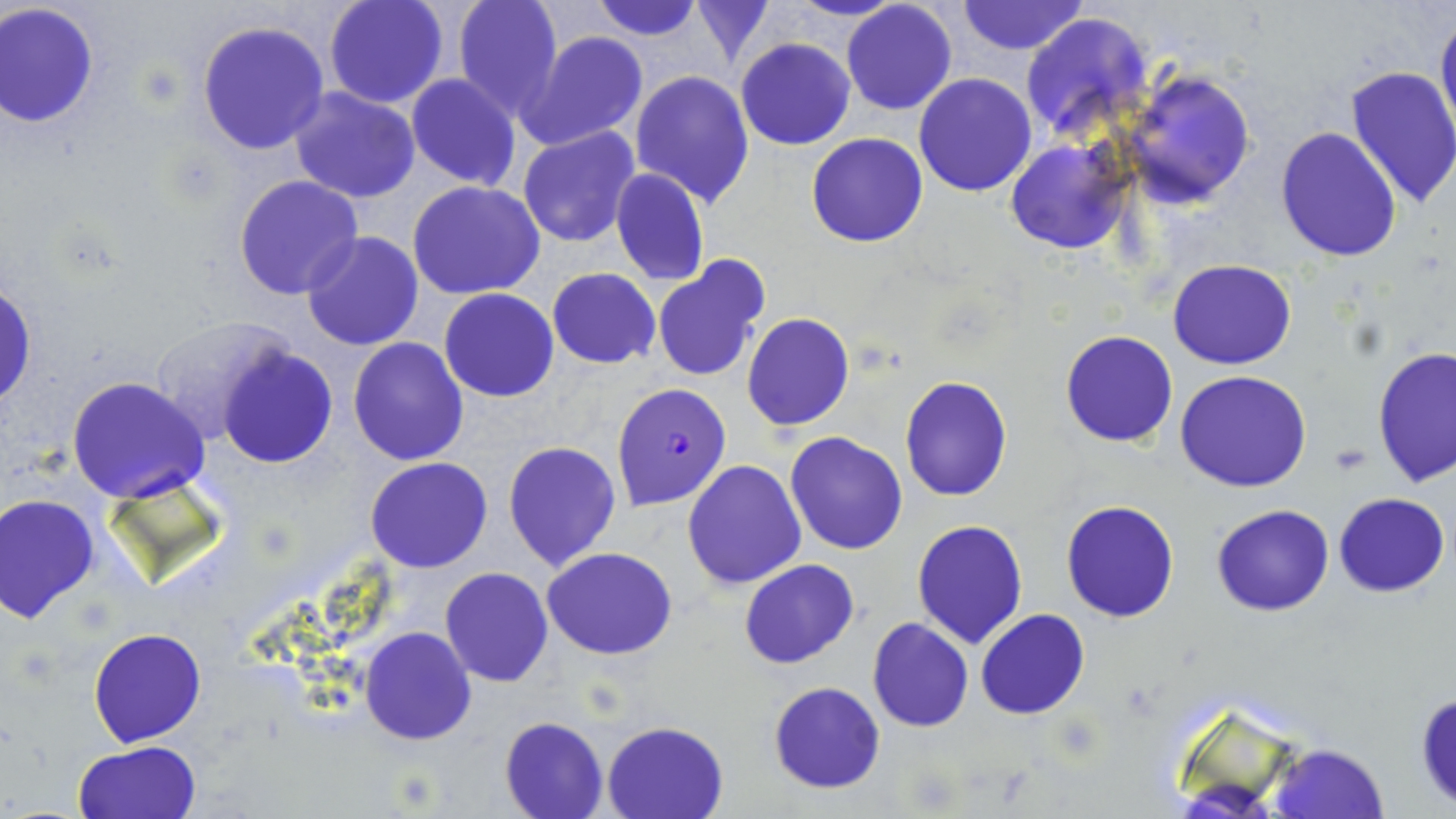

{
  "slide_level_diagnosis": "Plasmodium falciparum",
  "modality": "light microscopy",
  "stain": "May-Grünwald-Giemsa",
  "image_size": "1456×819 pixels",
  "plasmodium_falciparum_infected_red_blood_cell_locations": "approximate bounding boxes as [x1, y1, x2, y2] in pixels: [612, 382, 731, 509]",
  "field_of_view": "one of a larger specimen",
  "preparation": "thin blood film",
  "magnification": "1000x",
  "uninfected_red_blood_cell_locations": "approximate bounding boxes as [x1, y1, x2, y2] in pixels: [324, 0, 449, 108], [453, 0, 564, 119], [588, 0, 707, 42], [689, 0, 777, 68], [788, 0, 907, 22], [841, 1, 957, 116], [957, 1, 1088, 55], [0, 2, 101, 129], [1435, 7, 1456, 143], [1021, 11, 1156, 143], [196, 19, 330, 156], [518, 31, 650, 151], [736, 38, 855, 151], [1345, 66, 1456, 210], [630, 69, 755, 209], [1120, 70, 1256, 208], [915, 73, 1037, 194], [406, 74, 521, 190], [289, 86, 420, 204], [516, 126, 639, 248], [1275, 127, 1402, 264], [807, 133, 928, 247], [1006, 138, 1134, 255], [610, 168, 709, 287], [233, 175, 363, 300], [409, 182, 547, 299], [301, 231, 423, 351], [652, 257, 769, 382], [1169, 260, 1297, 369], [547, 267, 660, 370], [1, 280, 37, 410], [440, 288, 559, 402], [741, 313, 854, 432], [148, 316, 298, 443], [1060, 330, 1179, 448], [348, 337, 469, 466], [218, 344, 339, 469], [1372, 347, 1454, 489], [1174, 371, 1313, 494], [66, 376, 210, 504], [900, 376, 1012, 502], [784, 430, 909, 557], [502, 441, 622, 574], [366, 456, 492, 572], [682, 459, 807, 589], [1334, 492, 1451, 597], [0, 494, 99, 622], [1060, 499, 1180, 622], [1211, 504, 1335, 616], [912, 519, 1029, 649], [542, 547, 677, 659], [739, 558, 859, 669], [440, 567, 553, 687], [974, 609, 1089, 720], [867, 617, 973, 732], [359, 627, 477, 745], [88, 628, 206, 747], [768, 681, 886, 794], [1414, 689, 1456, 809], [499, 715, 609, 819], [601, 720, 730, 818], [72, 740, 202, 819], [1270, 744, 1388, 819]"
}